Describe the morphology of the red blood cells.
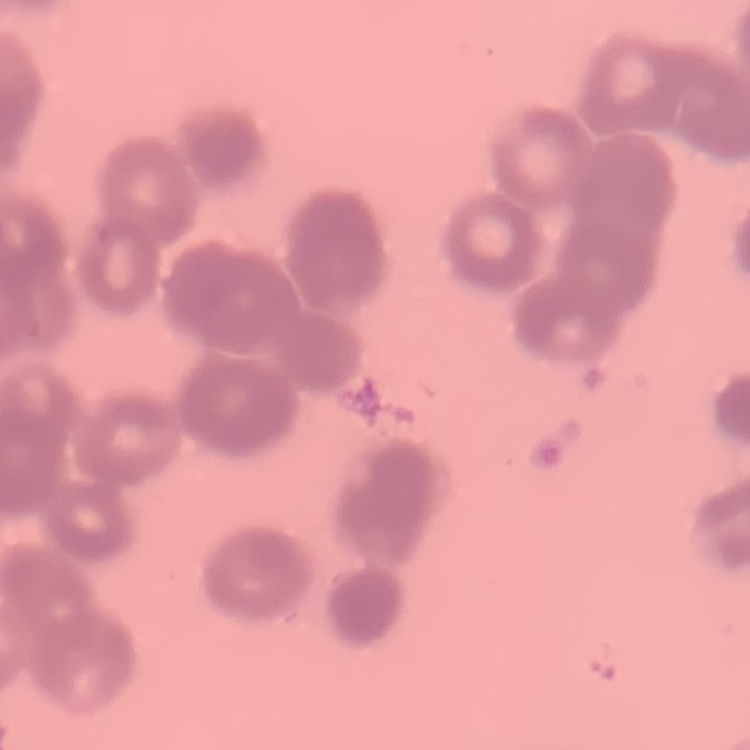

They show rouleaux formation.

stain: Field's or Giemsa
image_type: one tile cut from a larger photomicrograph
preparation: thin blood film